Report the malaria status.
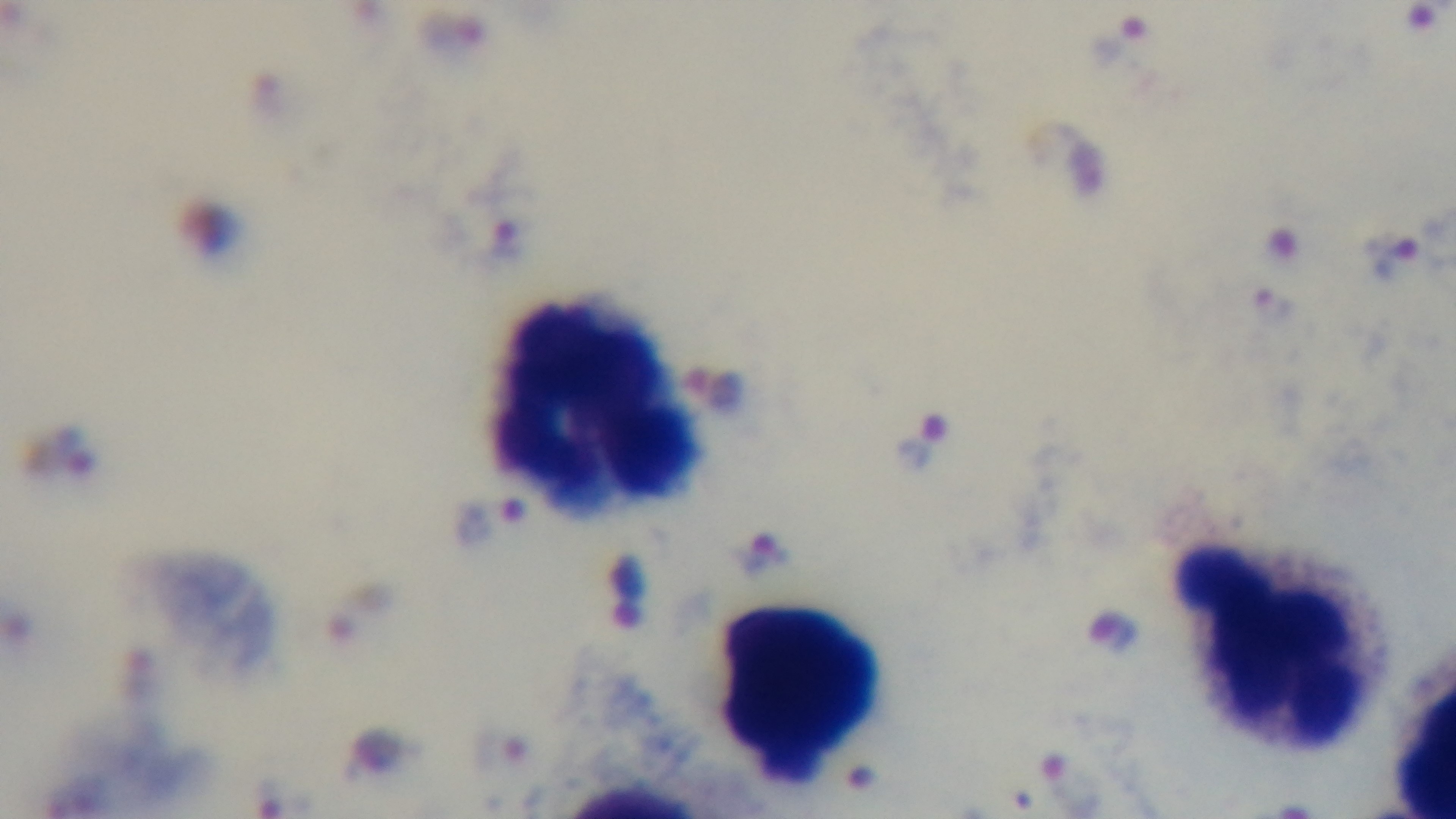

Infected.

Giemsa-stained. 100x oil-immersion objective. One field from the slide. Captured with a mounted 4K digital camera. Photomicrograph. Preparation: thick.